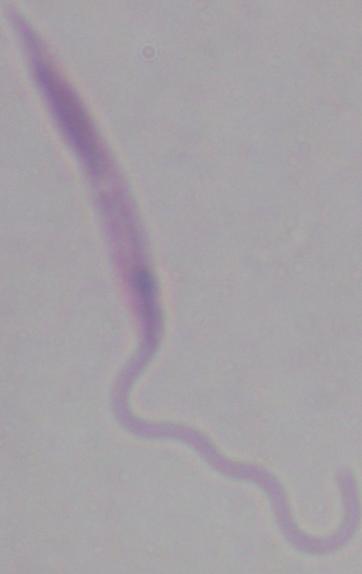
Summary:
  - Modality: photomicrograph
  - Identification: Leishmania
  - Magnification: 1000x